Locate every malaria parasite.
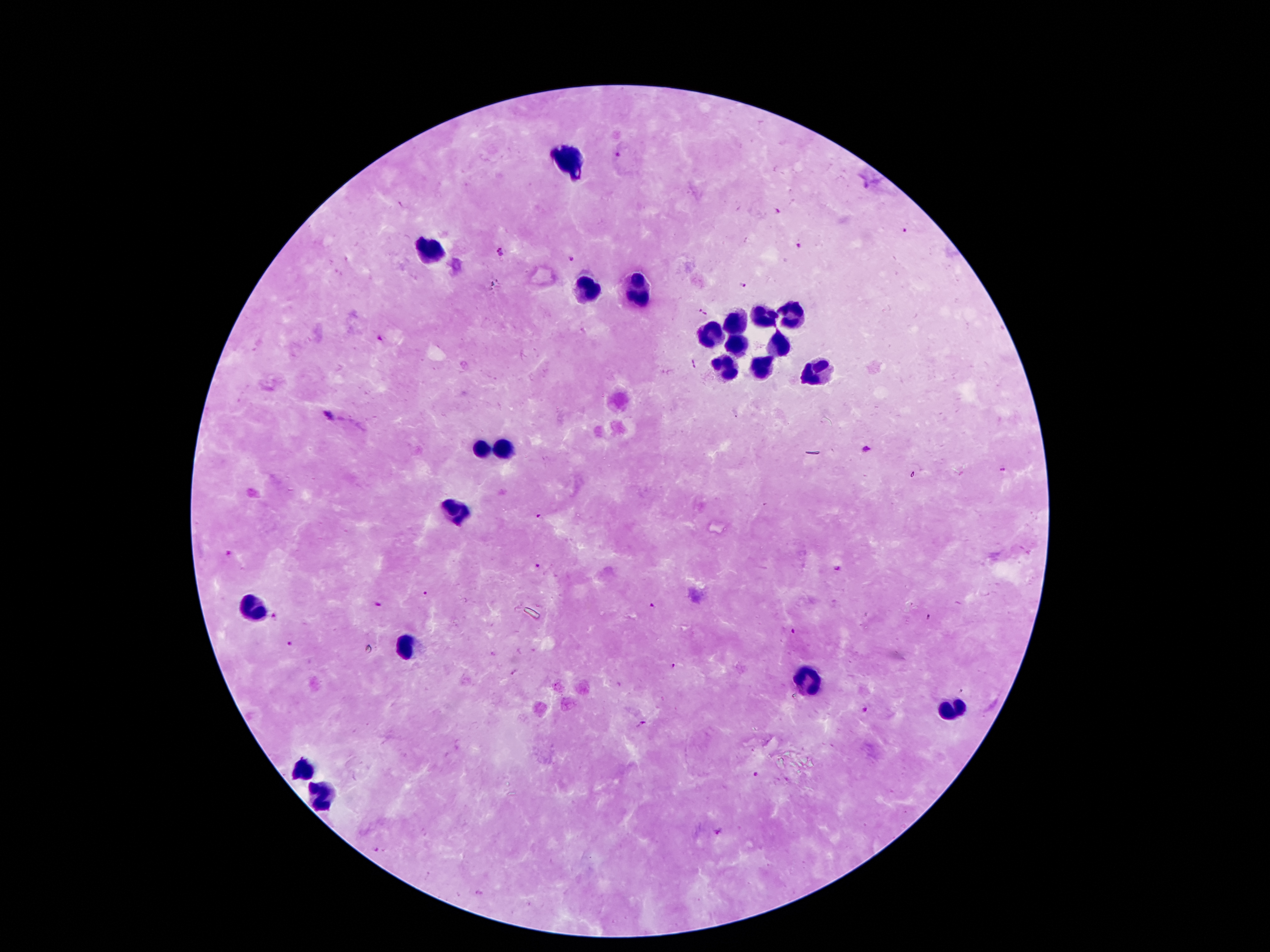
Approximate centers as {x, y} in pixels.
Malaria parasites: {617, 152}, {776, 212}, {904, 229}, {799, 247}, {497, 253}, {569, 260}, {743, 285}, {702, 310}, {379, 338}, {330, 415}, {867, 448}, {541, 516}, {230, 552}, {535, 566}, {836, 569}, {426, 595}, {377, 605}, {651, 606}, {926, 617}, {273, 618}, {793, 632}, {291, 643}, {673, 664}, {864, 709}, {642, 723}, {757, 773}, {717, 831}, {375, 849}, {478, 892}.

leukocyte_locations: 'approximate centers as {x, y} in pixels: {570, 163}, {433, 247}, {585, 288}, {637, 290}, {793, 315}, {762, 317}, {735, 326}, {711, 334}, {781, 345}, {736, 346}, {728, 369}, {762, 369}, {815, 374}, {506, 446}, {484, 451}, {455, 513}, {252, 608}, {409, 646}, {805, 681}, {953, 710}, {303, 765}, {316, 796}'
patient_malaria_status: positive for Plasmodium falciparum
preparation: thick blood smear
stain: Giemsa
magnification: 100x
field_of_view: single
image_size: 1270×952 pixels
capture: smartphone camera through the microscope eyepiece